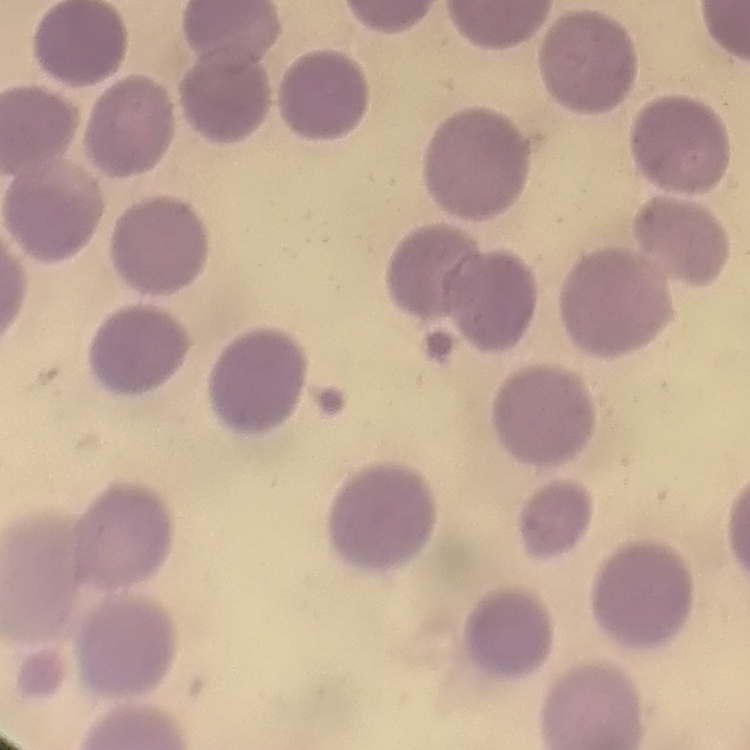

The red blood cells exhibit no rouleaux formation. Thin peripheral smear. Stained with either Field's or Giemsa. One tile cut from a larger photomicrograph.